Assess the morphology of the red blood cells.
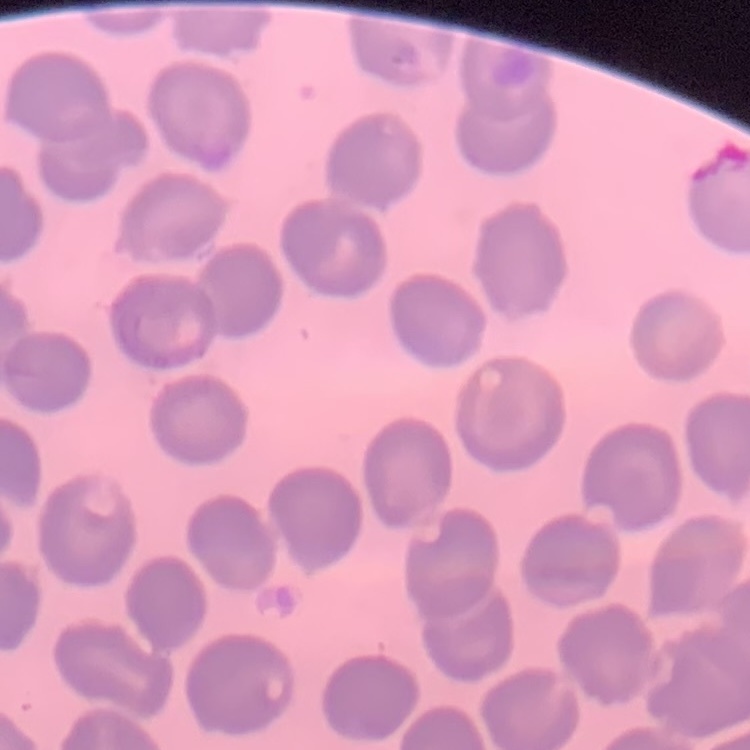
They show no rouleaux formation.

Thin blood film. One tile cut from a larger photomicrograph. Stained with either Field's or Giemsa.